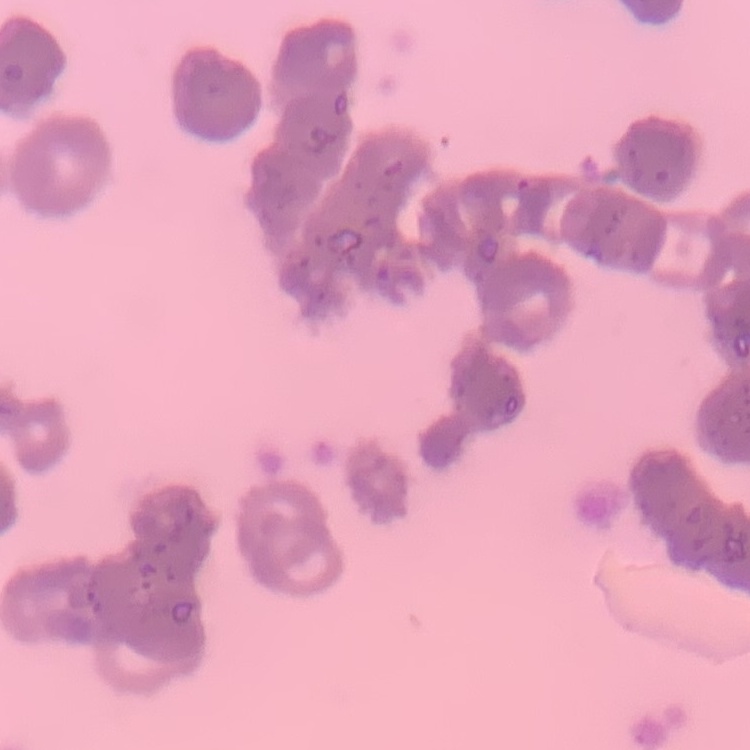
red blood cell morphology = rouleaux formation
preparation = thin peripheral smear
image type = square crop of a larger photomicrograph
stain = Field's or Giemsa